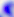

identification: Toxoplasma gondii
modality: photomicrograph
magnification: 400x